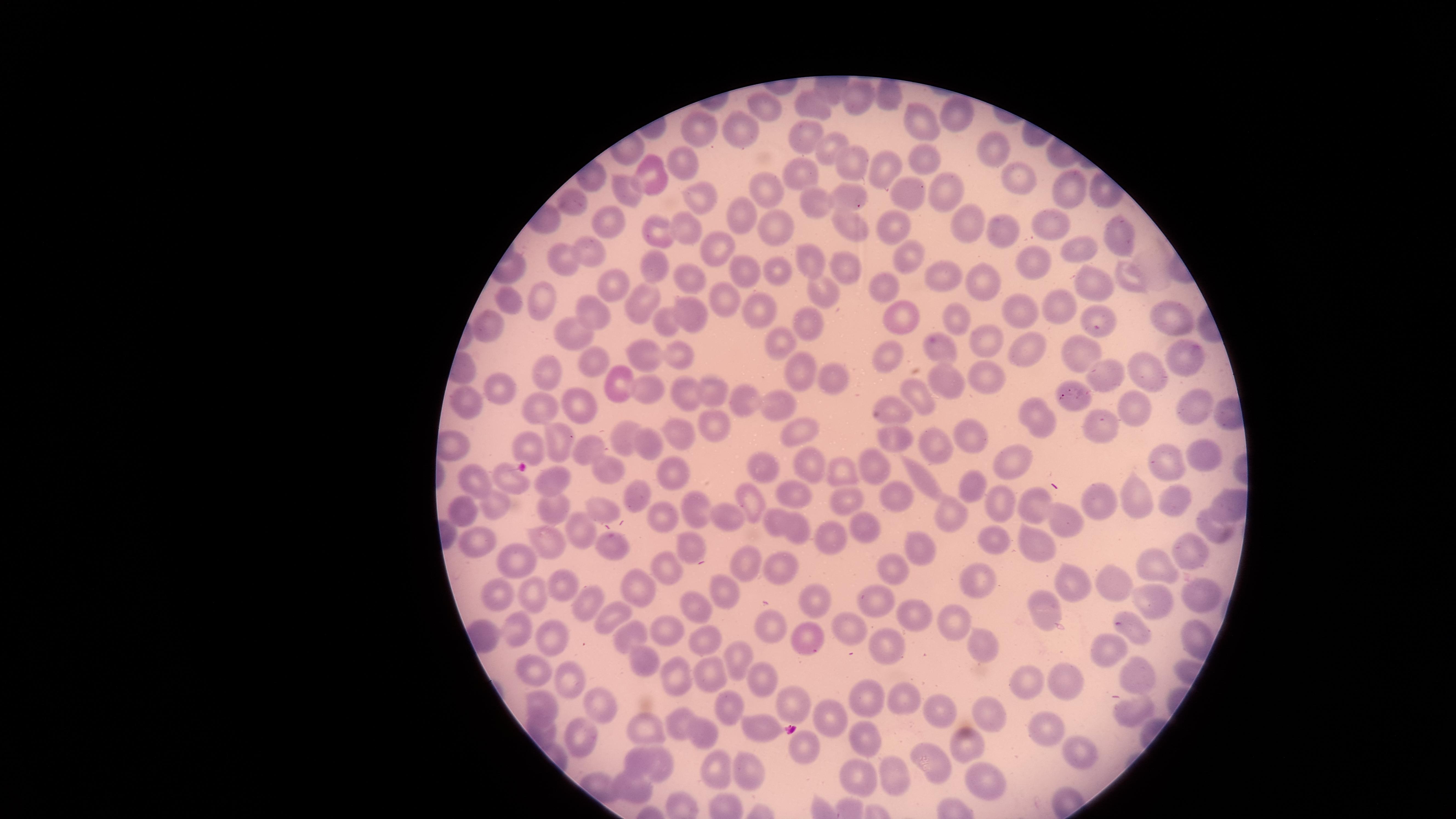
{
  "stain": "Giemsa",
  "presence": "no malaria parasites identified",
  "visible_region": "circular",
  "preparation": "thin smear of blood",
  "field_of_view": "single",
  "capture": "smartphone photograph through the microscope eyepiece",
  "image_size": "1456×819 pixels",
  "uninfected_red_blood_cells": "approximate marker points as {x, y} in pixels: {892, 97}, {855, 98}, {762, 99}, {812, 103}, {961, 114}, {918, 123}, {739, 132}, {708, 133}, {807, 137}, {991, 144}, {825, 151}, {924, 158}, {680, 162}, {883, 166}, {849, 167}, {799, 170}, {646, 175}, {1026, 176}, {761, 184}, {618, 188}, {1073, 191}, {913, 192}, {953, 192}, {693, 197}, {859, 198}, {819, 202}, {576, 206}, {744, 215}, {969, 220}, {1047, 220}, {608, 223}, {846, 225}, {892, 227}, {777, 230}, {685, 231}, {1121, 233}, {666, 234}, {1007, 236}, {714, 247}, {590, 252}, {912, 252}, {1079, 254}, {559, 255}, {812, 255}, {843, 262}, {1043, 262}, {654, 268}, {778, 268}, {745, 270}, {948, 273}, {1131, 274}, {692, 275}, {614, 283}, {886, 284}, {988, 284}, {1099, 286}, {823, 295}, {505, 300}, {725, 300}, {761, 300}, {547, 303}, {648, 303}, {1067, 307}, {593, 309}, {697, 312}, {1029, 314}, {906, 316}, {955, 316}, {1162, 316}, {488, 320}, {804, 320}, {667, 321}, {1087, 326}, {568, 329}, {993, 337}, {781, 342}, {941, 344}, {1033, 344}, {676, 349}, {1083, 353}, {1191, 354}, {646, 355}, {892, 358}, {589, 359}, {543, 368}, {1142, 370}, {798, 371}, {1115, 372}, {989, 374}, {833, 375}, {950, 376}, {621, 384}, {709, 386}, {503, 388}, {651, 392}, {922, 395}, {691, 396}, {744, 396}, {1074, 396}, {458, 401}, {778, 402}, {538, 406}, {1133, 406}, {1195, 408}, {584, 409}, {891, 409}, {1038, 414}, {709, 423}, {1094, 426}, {680, 431}, {974, 431}, {808, 432}, {555, 435}, {627, 435}, {897, 440}, {587, 444}, {932, 444}, {449, 445}, {650, 445}, {526, 447}, {1204, 455}, {1165, 457}, {759, 462}, {1015, 463}, {878, 467}, {814, 469}, {844, 469}, {604, 472}, {673, 474}, {926, 479}, {511, 482}, {558, 482}, {977, 483}, {472, 485}, {636, 490}, {785, 491}, {900, 495}, {845, 497}, {1003, 497}, {1131, 498}, {1227, 501}, {757, 502}, {1097, 503}, {552, 504}, {1041, 504}, {490, 505}, {1175, 505}, {601, 506}, {462, 511}, {693, 513}, {729, 515}, {953, 515}, {1066, 517}, {664, 518}, {864, 520}, {770, 521}, {1211, 523}, {800, 528}, {833, 532}, {990, 534}, {583, 535}, {688, 536}, {548, 538}, {1033, 542}, {482, 543}, {617, 545}, {918, 549}, {1185, 551}, {517, 557}, {1158, 561}, {745, 563}, {780, 563}, {898, 569}, {663, 570}, {975, 579}, {1072, 579}, {1112, 581}, {563, 582}, {719, 587}, {497, 591}, {642, 591}, {533, 592}, {1200, 597}, {1150, 599}, {809, 603}, {881, 605}, {590, 606}, {611, 608}, {699, 608}, {1045, 613}, {915, 614}, {953, 619}, {849, 625}, {1132, 625}, {771, 628}, {525, 632}, {663, 632}, {808, 633}, {546, 634}, {622, 637}, {702, 637}, {983, 643}, {884, 647}, {1109, 652}, {733, 659}, {642, 664}, {1148, 670}, {527, 671}, {715, 671}, {673, 672}, {764, 674}, {1063, 675}, {565, 677}, {1021, 682}, {869, 695}, {602, 697}, {801, 700}, {906, 700}, {728, 704}, {545, 705}, {937, 713}, {1132, 714}, {833, 715}, {986, 716}, {758, 725}, {679, 727}, {1048, 727}, {578, 729}, {649, 729}, {543, 730}, {860, 735}, {705, 737}, {966, 744}, {800, 747}, {1080, 751}, {629, 756}, {930, 756}, {660, 762}, {712, 768}, {853, 768}, {891, 770}, {748, 776}, {978, 779}, {633, 790}"
}